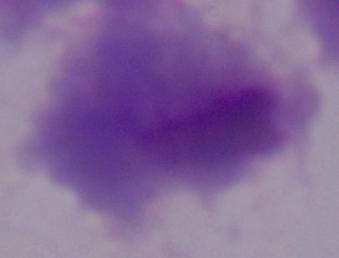 1000x magnification. A trichomonad is seen. Photomicrograph.